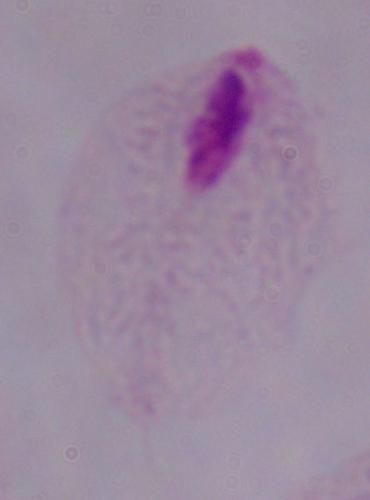

identification = trichomonad
modality = photomicrograph
magnification = 1000x